Locate every Plasmodium ovale-infected red blood cell.
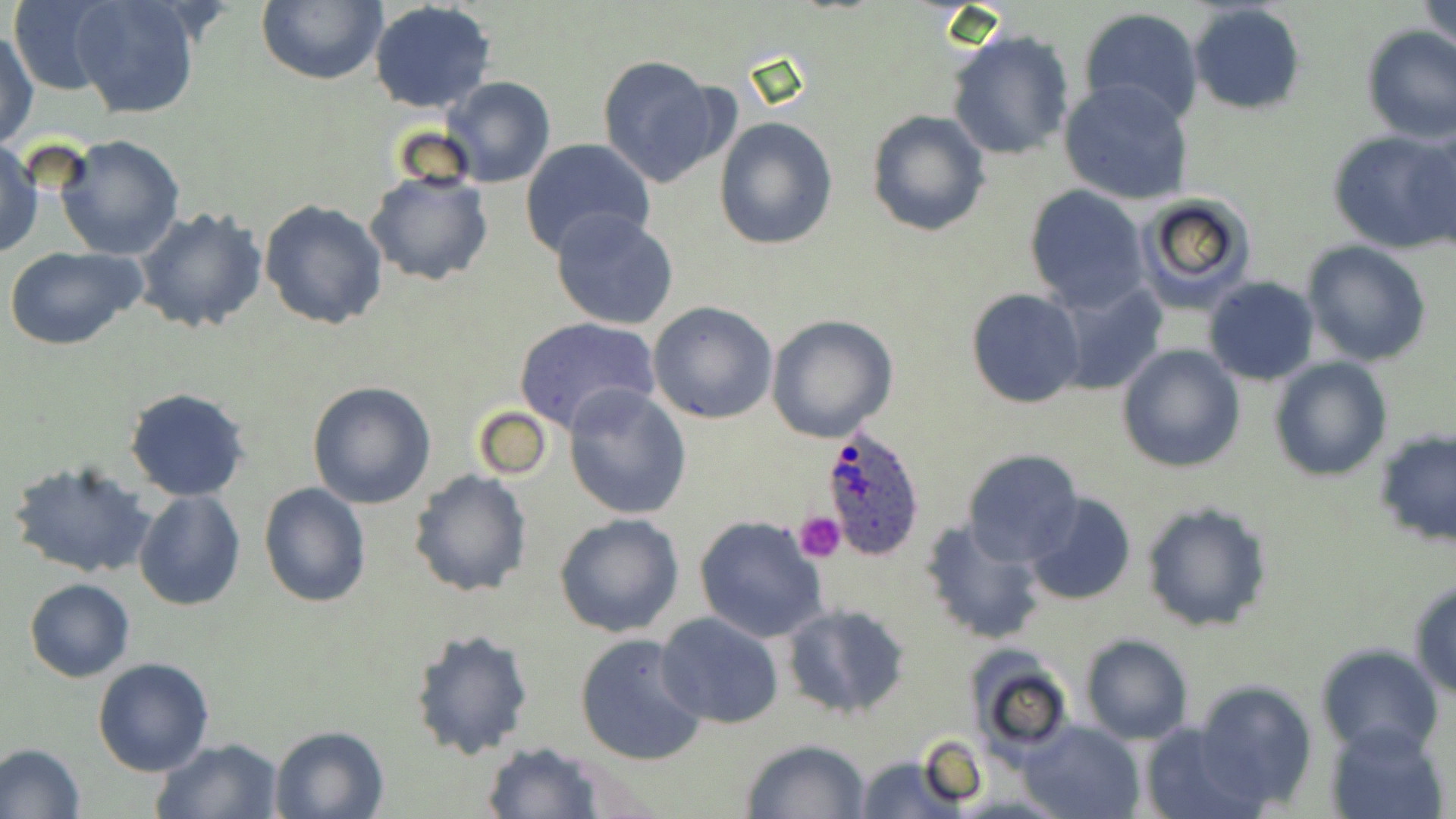
Approximate bounding boxes as named x1/y1/x2/y2 corners in pixels.
Plasmodium ovale-infected red blood cells: (x1=818, y1=423, x2=928, y2=559).

Platelet locations: (x1=796, y1=510, x2=846, y2=562). Uninfected red blood cell locations: (x1=255, y1=0, x2=386, y2=86), (x1=369, y1=0, x2=495, y2=113), (x1=1422, y1=0, x2=1455, y2=58), (x1=9, y1=1, x2=114, y2=95), (x1=71, y1=1, x2=200, y2=120), (x1=1187, y1=3, x2=1308, y2=115), (x1=1078, y1=8, x2=1205, y2=126), (x1=948, y1=27, x2=1074, y2=161), (x1=1361, y1=27, x2=1456, y2=144), (x1=1, y1=29, x2=38, y2=150), (x1=595, y1=54, x2=729, y2=187), (x1=442, y1=76, x2=554, y2=187), (x1=1059, y1=80, x2=1195, y2=206), (x1=866, y1=110, x2=991, y2=238), (x1=714, y1=117, x2=839, y2=250), (x1=1406, y1=126, x2=1456, y2=253), (x1=1328, y1=127, x2=1456, y2=255), (x1=56, y1=134, x2=185, y2=260), (x1=519, y1=137, x2=656, y2=258), (x1=1, y1=140, x2=43, y2=259), (x1=364, y1=169, x2=494, y2=287), (x1=1023, y1=186, x2=1149, y2=313), (x1=1133, y1=194, x2=1257, y2=312), (x1=258, y1=199, x2=389, y2=331), (x1=134, y1=207, x2=268, y2=335), (x1=550, y1=208, x2=680, y2=330), (x1=1301, y1=239, x2=1433, y2=366), (x1=3, y1=245, x2=148, y2=350), (x1=1201, y1=276, x2=1321, y2=386), (x1=1053, y1=279, x2=1167, y2=395), (x1=966, y1=287, x2=1086, y2=409), (x1=648, y1=300, x2=779, y2=424), (x1=766, y1=315, x2=898, y2=444), (x1=513, y1=316, x2=662, y2=435), (x1=1117, y1=344, x2=1245, y2=473), (x1=1269, y1=356, x2=1393, y2=480), (x1=307, y1=381, x2=437, y2=509), (x1=563, y1=385, x2=691, y2=520), (x1=124, y1=388, x2=251, y2=501), (x1=470, y1=405, x2=552, y2=480), (x1=1376, y1=434, x2=1454, y2=547), (x1=961, y1=447, x2=1085, y2=565), (x1=6, y1=457, x2=158, y2=581), (x1=408, y1=470, x2=533, y2=598), (x1=258, y1=481, x2=371, y2=607), (x1=133, y1=490, x2=247, y2=611), (x1=1024, y1=492, x2=1136, y2=607), (x1=1141, y1=500, x2=1276, y2=633), (x1=553, y1=513, x2=684, y2=638), (x1=694, y1=515, x2=829, y2=644), (x1=920, y1=519, x2=1048, y2=646), (x1=25, y1=578, x2=135, y2=682), (x1=1408, y1=579, x2=1456, y2=699), (x1=780, y1=603, x2=914, y2=718), (x1=655, y1=611, x2=785, y2=730), (x1=408, y1=627, x2=533, y2=759), (x1=574, y1=633, x2=710, y2=767), (x1=1080, y1=634, x2=1194, y2=744), (x1=1314, y1=643, x2=1443, y2=754), (x1=965, y1=652, x2=1075, y2=757), (x1=92, y1=657, x2=215, y2=775), (x1=1192, y1=679, x2=1321, y2=810), (x1=1018, y1=720, x2=1145, y2=819), (x1=1138, y1=720, x2=1263, y2=819), (x1=1328, y1=721, x2=1450, y2=819), (x1=269, y1=725, x2=389, y2=819), (x1=150, y1=737, x2=285, y2=819), (x1=740, y1=738, x2=872, y2=819), (x1=0, y1=742, x2=85, y2=818), (x1=480, y1=742, x2=609, y2=818), (x1=856, y1=754, x2=961, y2=818). Slide-level diagnosis: Plasmodium ovale. Image is 1456×819 pixels. Thin blood film. May-Grünwald-Giemsa stain. 1000x magnification. Optical microscopy. One field of a larger specimen.